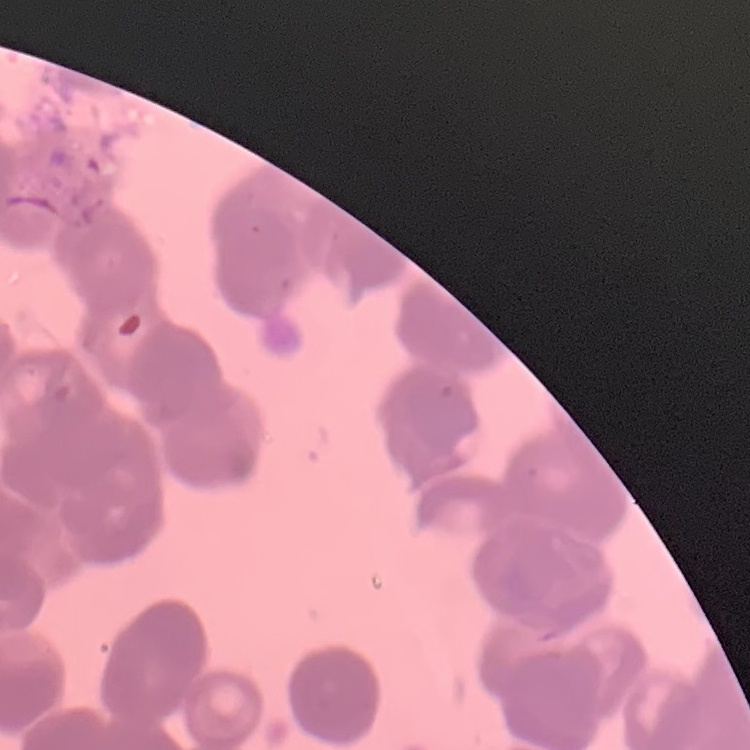
The erythrocytes show rouleaux formation. Field's or Giemsa stain. Thin blood smear. One tile cut from a larger photomicrograph.